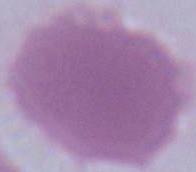
Photomicrograph. Captured at 1000x magnification. A red blood cell is seen.